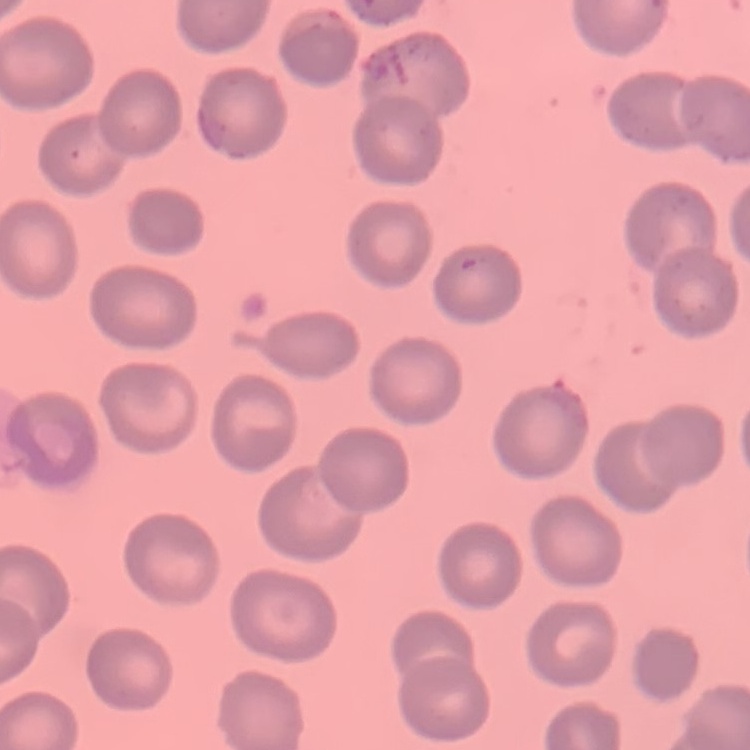
The erythrocytes exhibit no rouleaux formation. Stained with either Field's or Giemsa. Square crop of a larger photomicrograph. Thin blood film.